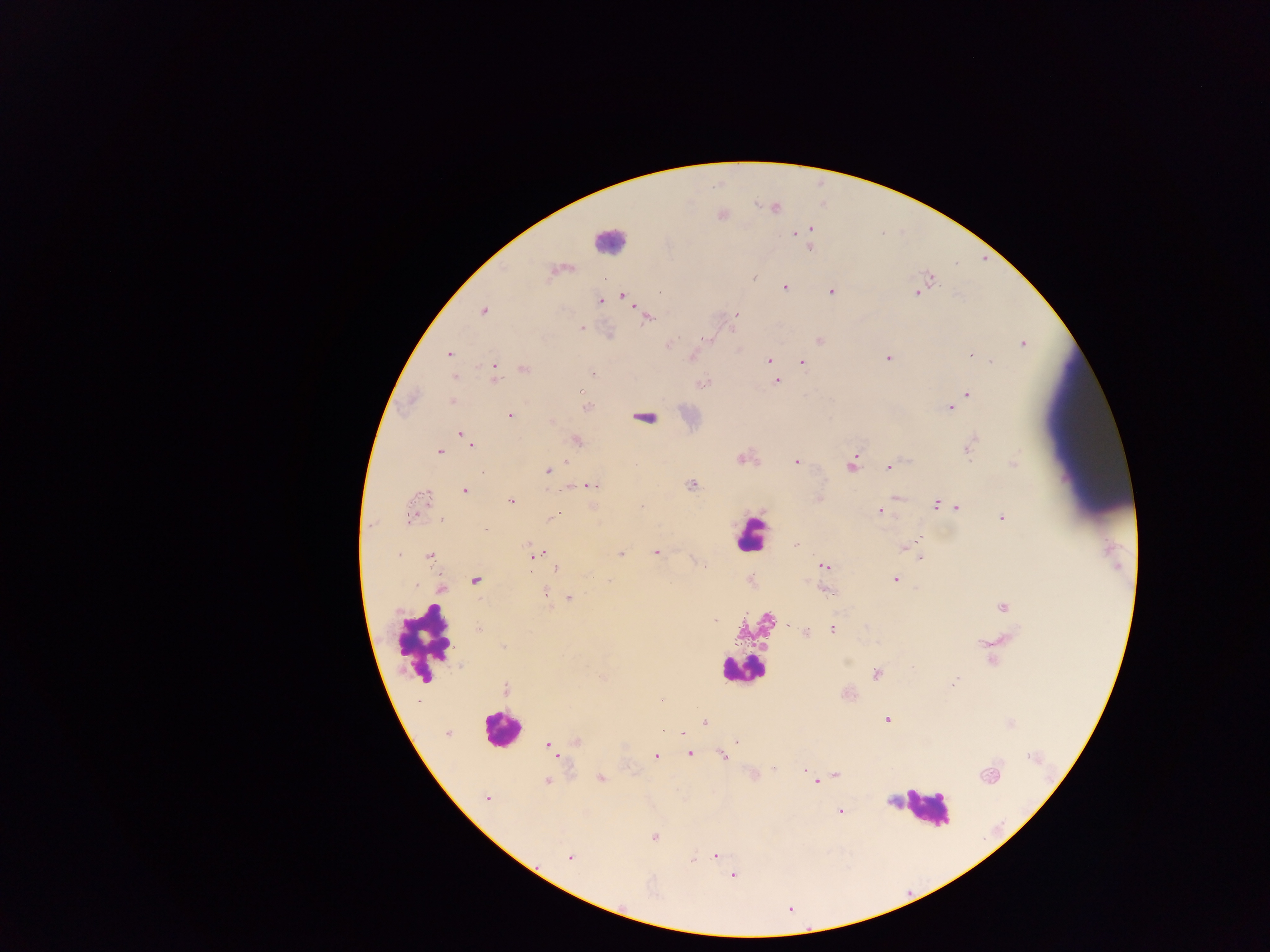
field of view = single
preparation = thick blood film
image size = 1270×952 pixels
leukocyte locations = approximate centers as [x, y] in pixels: [609, 240], [751, 535], [426, 639], [740, 669], [500, 729], [925, 806]
capture = mobile-phone photograph through a microscope
country = Ghana
Plasmodium parasite locations = approximate centers as [x, y] in pixels: [774, 207], [811, 229], [796, 233], [809, 249], [551, 272], [753, 277], [931, 278], [784, 287], [831, 291], [915, 292], [623, 295], [600, 301], [484, 310], [736, 314], [647, 318], [580, 328], [734, 329], [708, 340], [819, 340], [1023, 343], [669, 344], [449, 354], [692, 356], [969, 356], [887, 358], [769, 360], [991, 361], [802, 362], [771, 364], [525, 369], [495, 372], [593, 372], [455, 377], [777, 382], [702, 383], [580, 391], [967, 395], [452, 401], [586, 407], [950, 408], [510, 415], [645, 418], [460, 433], [577, 440], [971, 443], [471, 444], [968, 450], [439, 451], [741, 459], [796, 461], [1013, 462], [566, 463], [852, 464], [889, 467], [553, 468], [548, 470], [483, 473], [591, 485], [691, 485], [465, 490], [427, 496], [896, 496], [510, 501], [936, 505], [641, 507], [957, 508], [880, 512], [412, 515], [555, 516], [1002, 518], [440, 519], [919, 538], [915, 541], [796, 545], [904, 548], [527, 549], [656, 552], [541, 553], [399, 554], [533, 555], [620, 555], [429, 557], [920, 558], [703, 565], [824, 566], [557, 569], [475, 580], [609, 580], [895, 580], [416, 585], [443, 588], [825, 590], [545, 593], [569, 598], [1003, 607], [715, 619], [766, 620], [789, 625], [478, 629], [832, 629], [806, 633], [503, 647], [913, 668], [876, 674], [952, 683], [505, 688], [661, 700], [887, 719], [704, 722], [662, 730], [448, 733], [576, 741], [736, 742], [549, 746], [690, 753], [556, 755], [722, 756], [656, 757], [774, 770], [805, 770], [836, 775], [989, 775], [601, 778], [546, 781], [815, 782], [487, 798], [840, 811], [655, 837], [715, 855], [570, 857], [693, 860], [733, 875]